Give the position of every Plasmodium parasite.
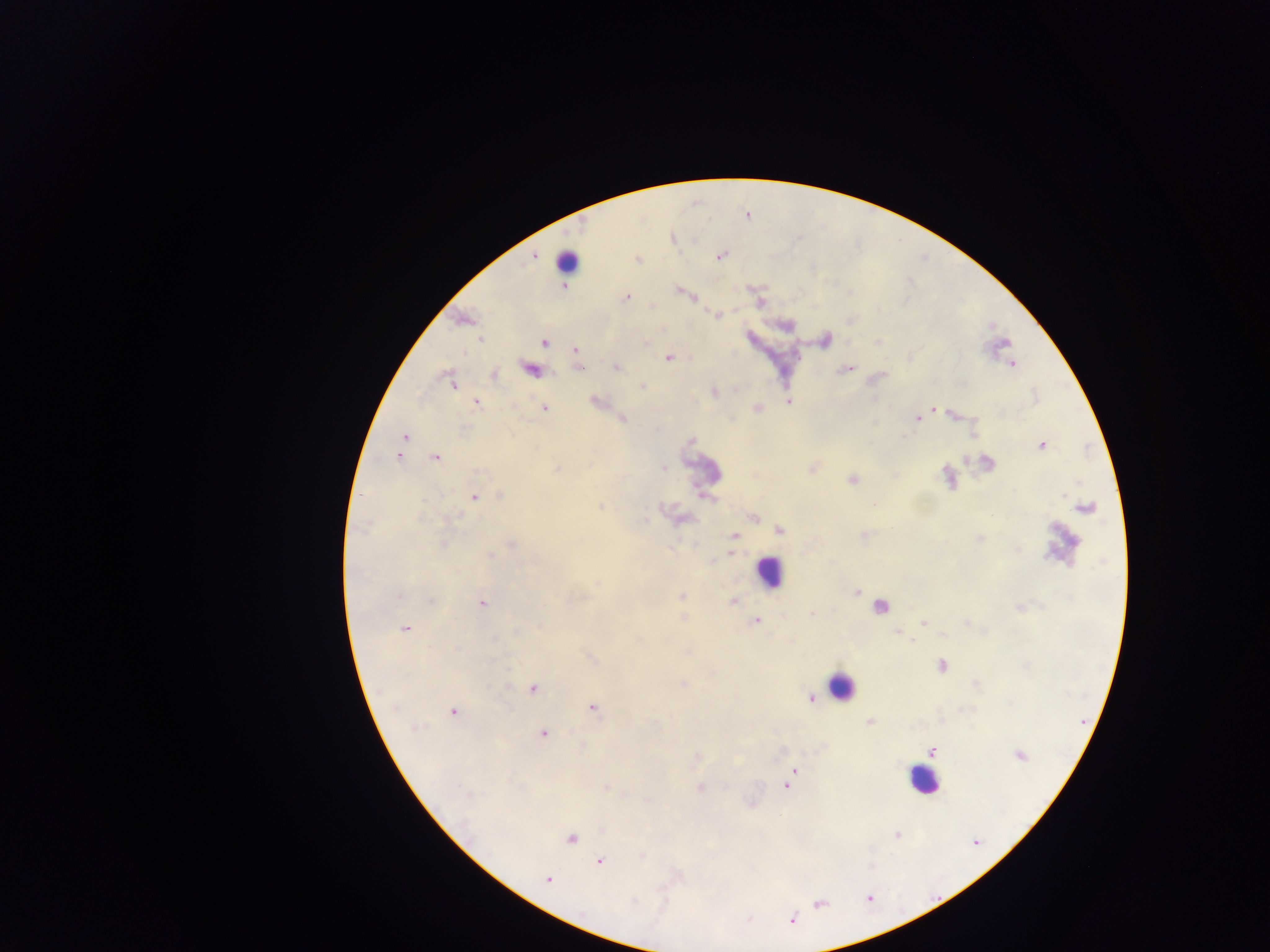

Approximate centers as (x, y) in pixels.
Plasmodium parasites: (627, 297), (480, 339), (545, 342), (574, 350), (668, 358), (1012, 364), (494, 375), (452, 383), (789, 402), (477, 403), (544, 408), (932, 409), (918, 418), (405, 436), (1042, 445), (398, 456), (434, 458), (474, 497), (490, 555), (430, 601), (734, 602), (482, 603), (757, 620), (405, 629), (912, 640), (533, 689), (811, 699), (592, 708), (453, 712), (869, 722), (544, 733), (932, 751), (1019, 755), (794, 770), (788, 784), (571, 838), (600, 861), (548, 879).

Leukocyte locations: (569, 260), (768, 571), (840, 685), (923, 780). One field of view. Image is 1270×952 pixels. Collected in Ghana. Mobile-phone photograph taken through the microscope. Thick blood film.